Assess the morphology of the erythrocytes.
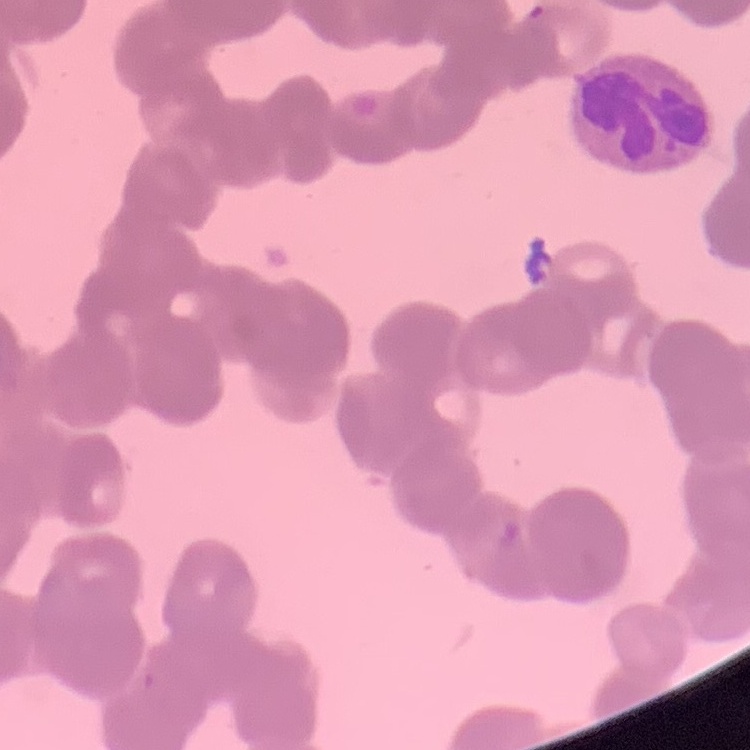

Rouleaux formation.

Summary:
  - Preparation: thin blood film
  - Image type: one tile cut from a larger photomicrograph
  - Stain: Field's or Giemsa